Locate every blood parasite and identify its species.
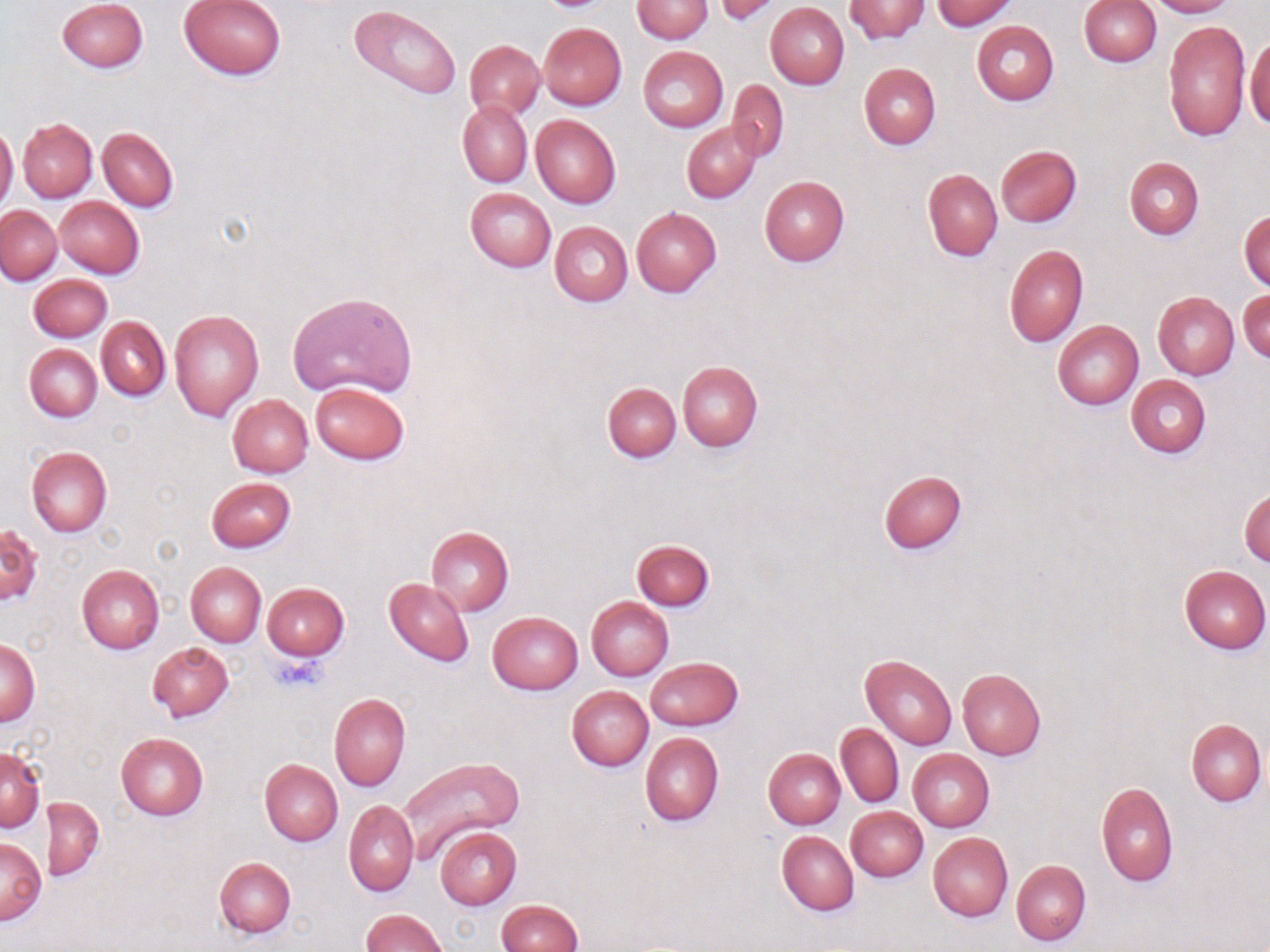
No blood parasites observed.

Summary:
  - Coordinate format: approximate bounding boxes as [x1, y1, x2, y2] in pixels
  - Uninfected red blood cell locations: [56, 0, 148, 73], [178, 0, 286, 80], [631, 0, 713, 43], [845, 0, 930, 43], [928, 0, 1018, 31], [1148, 0, 1235, 18], [715, 1, 781, 26], [1079, 1, 1161, 66], [765, 3, 849, 89], [348, 5, 461, 101], [1163, 19, 1252, 141], [972, 21, 1059, 105], [539, 22, 627, 110], [1246, 37, 1270, 131], [464, 39, 544, 120], [638, 46, 729, 132], [858, 63, 941, 149], [727, 79, 788, 160], [458, 101, 532, 187], [531, 115, 620, 209], [18, 118, 97, 202], [681, 123, 760, 203], [0, 124, 18, 211], [98, 127, 179, 211], [995, 145, 1082, 227], [1123, 157, 1204, 239], [923, 169, 1003, 262], [759, 176, 850, 266], [465, 187, 555, 272], [54, 197, 144, 278], [1, 205, 61, 284], [631, 207, 721, 296], [1239, 211, 1269, 290], [550, 221, 632, 307], [1002, 244, 1089, 346], [28, 274, 112, 342], [1238, 288, 1270, 363], [285, 290, 418, 400], [1152, 292, 1238, 380], [169, 310, 264, 422], [97, 316, 170, 401], [1053, 321, 1143, 409], [24, 344, 102, 422], [677, 362, 763, 452], [1126, 375, 1211, 459], [602, 381, 681, 463], [311, 382, 409, 465], [227, 394, 314, 477], [26, 446, 112, 538], [878, 469, 967, 555], [206, 476, 296, 553], [1240, 490, 1269, 567], [0, 524, 41, 605], [426, 526, 513, 616], [631, 539, 714, 611], [185, 562, 265, 648], [1178, 564, 1269, 654], [76, 565, 165, 653], [384, 578, 473, 667], [261, 583, 348, 660], [586, 596, 673, 681], [488, 611, 582, 695], [1, 637, 40, 727], [147, 641, 234, 722], [861, 654, 956, 750], [646, 657, 742, 730], [957, 668, 1046, 760], [567, 685, 653, 771], [328, 693, 411, 791], [1186, 719, 1266, 806], [836, 724, 904, 807], [115, 731, 209, 819], [640, 733, 724, 826], [1, 747, 45, 833], [763, 748, 845, 828], [907, 749, 994, 831], [396, 755, 523, 864], [260, 759, 342, 846], [1096, 782, 1178, 886], [45, 796, 104, 881], [344, 800, 418, 897], [847, 806, 928, 882], [434, 826, 522, 910], [776, 831, 859, 917], [928, 832, 1012, 922], [0, 836, 45, 925], [213, 857, 296, 939], [1012, 859, 1091, 946], [495, 900, 583, 952], [359, 910, 449, 952]
  - Platelet locations: [270, 654, 326, 693]
  - Slide-level diagnosis: no evidence of blood parasites
  - Image size: 1270×952 pixels
  - Preparation: thin blood film
  - Magnification: 1000x
  - Field of view: single
  - Stain: May-Grünwald-Giemsa
  - Modality: optical microscopy